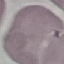
malaria status = uninfected
capture = smartphone camera at the microscope eyepiece
preparation = thin smear
stain = Giemsa
image type = cell patch, automatically extracted from a larger field of view and resized to 64 × 64 pixels